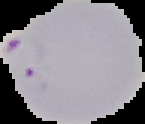

Segmented cell region on a black background. Image is 145×124 pixels. From a thin blood smear. Result: Plasmodium parasites detected.